Outline each blood parasite and name the species.
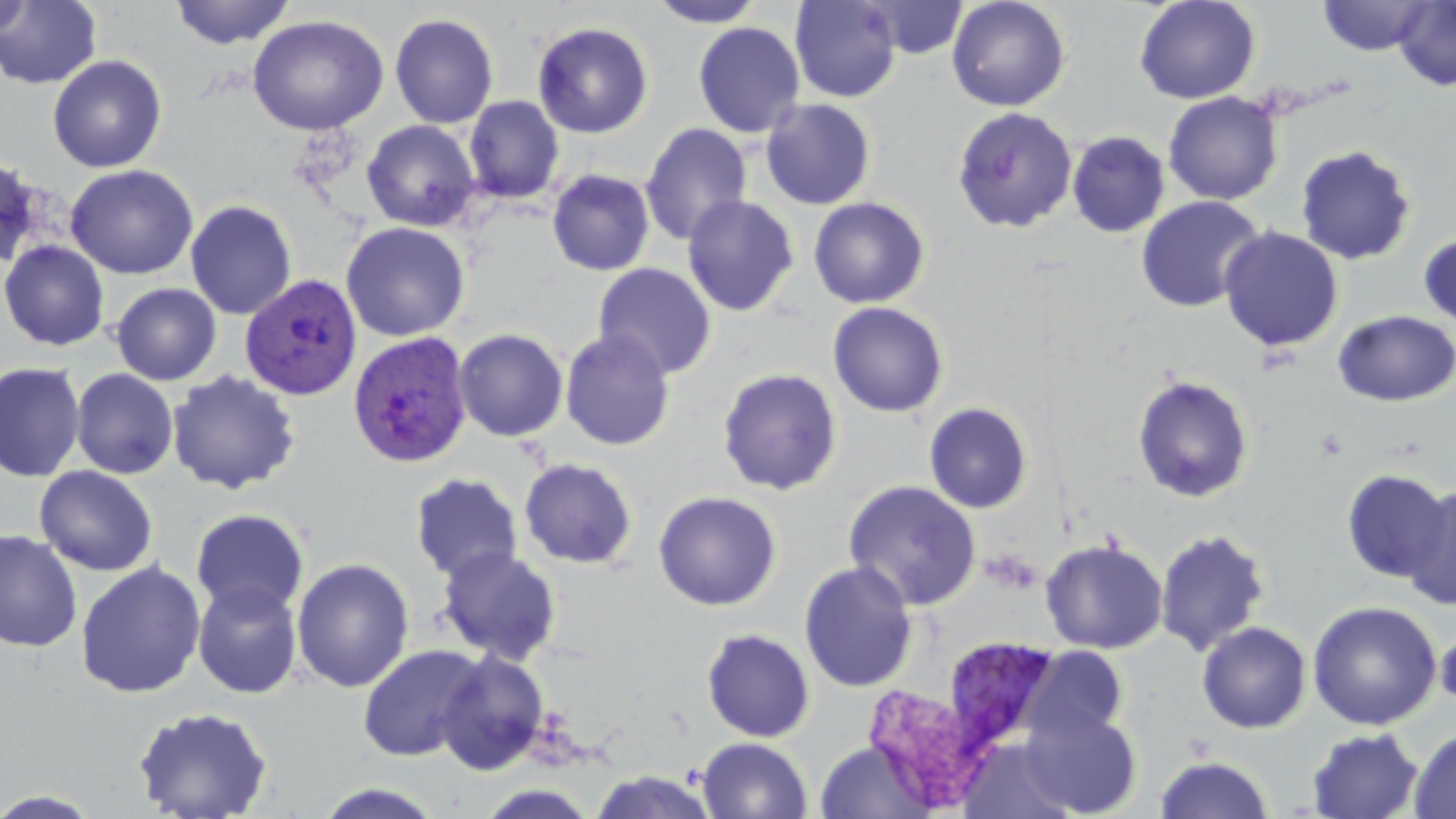

Approximate bounding boxes as [x1, y1, x2, y2] in pixels.
Plasmodium vivax-infected red blood cells: [240, 274, 363, 401], [348, 331, 474, 469], [938, 640, 1050, 765].
No Plasmodium falciparum, Plasmodium ovale, Plasmodium malariae, Babesia divergens, or Trypanosoma brucei observed.

slide-level diagnosis = Plasmodium vivax
preparation = thin blood film
platelet locations = approximate bounding boxes as [x1, y1, x2, y2] in pixels: [981, 549, 1041, 594]
field of view = one of a larger specimen
image size = 1456×819 pixels
modality = optical microscopy
uninfected red blood cell locations = approximate bounding boxes as [x1, y1, x2, y2] in pixels: [0, 0, 32, 39], [0, 0, 102, 89], [169, 0, 295, 50], [647, 0, 768, 27], [789, 0, 902, 103], [856, 0, 1039, 86], [859, 0, 969, 60], [946, 0, 1071, 112], [1134, 0, 1261, 104], [1317, 0, 1435, 56], [1393, 0, 1456, 91], [389, 12, 499, 129], [247, 14, 389, 136], [532, 21, 654, 139], [692, 22, 805, 138], [47, 54, 167, 173], [1163, 91, 1283, 206], [464, 95, 564, 205], [760, 98, 876, 210], [952, 106, 1078, 234], [361, 119, 482, 232], [639, 123, 753, 247], [1066, 131, 1170, 238], [1295, 144, 1416, 266], [0, 155, 42, 273], [64, 164, 198, 280], [546, 169, 655, 276], [682, 195, 799, 317], [1135, 195, 1265, 313], [808, 196, 930, 308], [185, 200, 297, 320], [341, 221, 470, 342], [1219, 225, 1345, 353], [1418, 232, 1456, 331], [0, 240, 110, 351], [592, 262, 717, 379], [111, 283, 222, 386], [827, 301, 949, 418], [1333, 310, 1456, 407], [453, 328, 569, 442], [560, 329, 676, 451], [0, 362, 85, 483], [717, 366, 843, 495], [71, 368, 178, 479], [166, 370, 301, 495], [1131, 374, 1255, 504], [923, 402, 1034, 514], [518, 458, 638, 570], [34, 465, 158, 577], [1341, 468, 1451, 583], [409, 472, 524, 584], [843, 479, 981, 610], [1401, 485, 1456, 612], [653, 490, 781, 611], [191, 508, 309, 619], [1154, 528, 1270, 657], [0, 529, 82, 653], [1040, 538, 1168, 654], [436, 546, 563, 666], [292, 557, 414, 693], [798, 560, 919, 693], [75, 562, 206, 699], [192, 579, 303, 699], [1307, 600, 1442, 730], [1196, 620, 1312, 734], [1435, 623, 1456, 715], [701, 628, 815, 743], [358, 645, 486, 761], [1022, 646, 1128, 745], [435, 650, 550, 775], [132, 705, 273, 819], [1020, 707, 1142, 818], [1305, 727, 1425, 819], [1409, 727, 1456, 818], [696, 737, 813, 819], [815, 741, 933, 819], [1154, 754, 1274, 819], [587, 770, 720, 819], [312, 782, 448, 819], [0, 789, 104, 818]
stain = May-Grünwald-Giemsa
magnification = 1000x